Locate every blood parasite and identify its species.
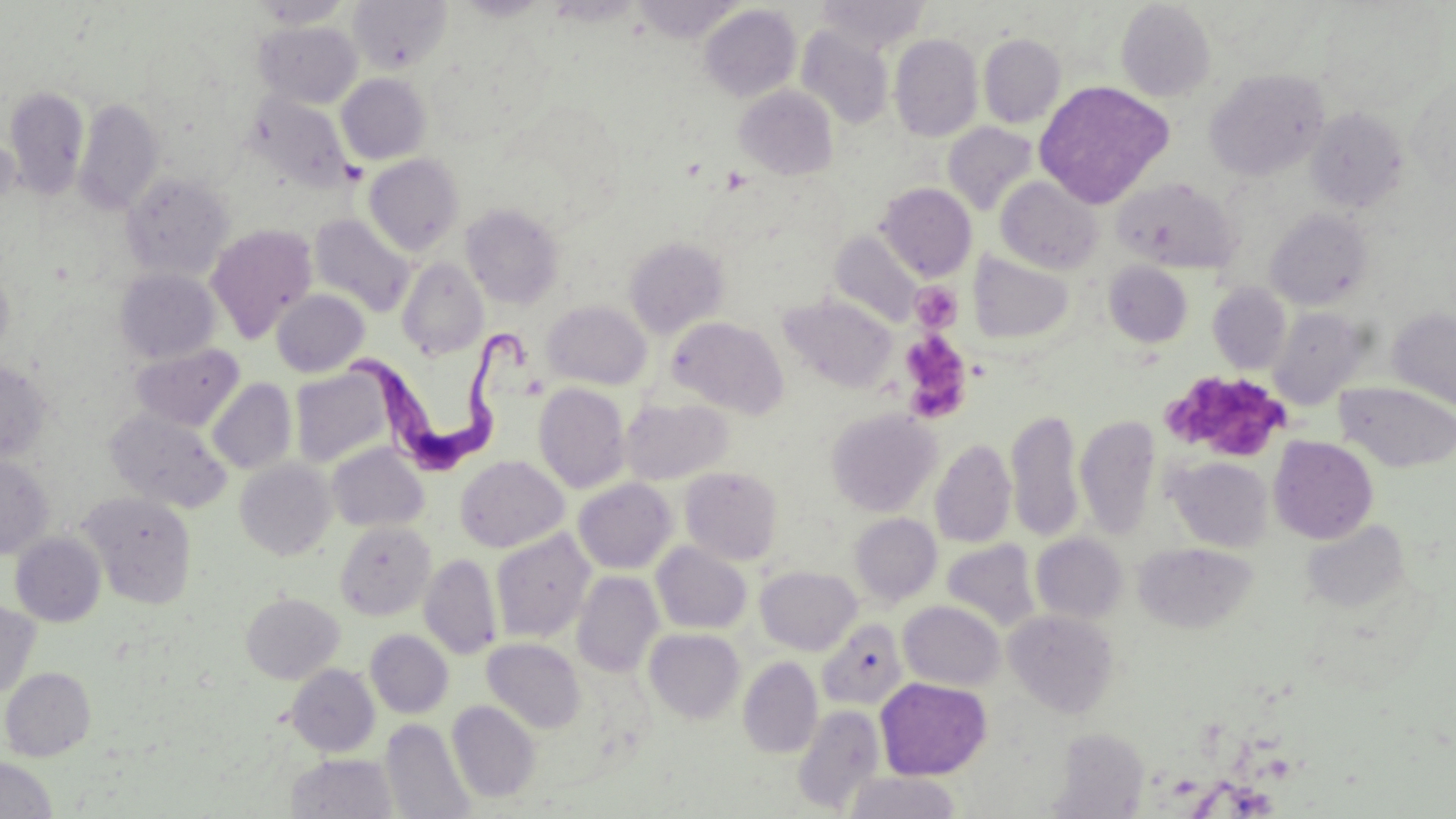

Approximate bounding boxes as (x1, y1, x2, y2) in pixels.
Trypanosoma brucei: (349, 321, 534, 475).
No Plasmodium falciparum, Plasmodium ovale, Plasmodium malariae, Plasmodium vivax, or Babesia divergens observed.

Summary:
  - Platelet locations: (909, 281, 962, 333), (898, 333, 972, 422), (1161, 373, 1294, 455)
  - Uninfected red blood cell locations: (348, 0, 452, 74), (633, 0, 746, 42), (818, 1, 931, 53), (1115, 1, 1215, 102), (699, 4, 801, 103), (1316, 4, 1445, 111), (254, 20, 363, 108), (796, 25, 894, 129), (978, 33, 1066, 128), (889, 34, 983, 142), (1204, 69, 1329, 181), (336, 73, 431, 165), (1406, 76, 1455, 190), (1033, 80, 1174, 208), (734, 85, 838, 180), (4, 86, 89, 199), (246, 93, 355, 193), (73, 97, 164, 215), (1306, 107, 1408, 213), (943, 122, 1038, 215), (364, 154, 464, 255), (121, 170, 234, 280), (995, 176, 1103, 274), (1113, 178, 1239, 274), (877, 182, 976, 281), (461, 203, 565, 309), (1266, 209, 1373, 309), (309, 213, 416, 317), (205, 224, 318, 341), (829, 231, 924, 328), (624, 236, 729, 338), (968, 251, 1076, 344), (396, 257, 489, 360), (1104, 261, 1193, 347), (0, 267, 13, 361), (115, 268, 220, 364), (1207, 282, 1292, 374), (271, 289, 369, 377), (781, 295, 897, 393), (542, 300, 652, 390), (1267, 306, 1372, 409), (1388, 308, 1456, 411), (666, 316, 788, 418), (131, 342, 244, 431), (0, 361, 53, 464), (290, 368, 393, 468), (207, 378, 297, 475), (1335, 381, 1456, 472), (533, 382, 630, 493), (620, 397, 732, 485), (825, 408, 941, 517), (1007, 408, 1084, 543), (106, 409, 231, 513), (1075, 414, 1160, 539), (1268, 436, 1378, 544), (930, 438, 1017, 548), (326, 443, 429, 532), (0, 455, 54, 559), (455, 455, 569, 553), (1166, 456, 1273, 552), (235, 458, 336, 560), (680, 467, 784, 564), (573, 478, 677, 574), (79, 491, 198, 608), (849, 513, 942, 607), (1300, 519, 1411, 613), (335, 521, 435, 620), (490, 529, 595, 643), (10, 532, 106, 627), (1031, 533, 1127, 624), (941, 538, 1041, 633), (651, 541, 752, 634), (1134, 542, 1258, 634), (419, 553, 502, 659), (756, 566, 862, 655), (572, 571, 663, 678), (241, 592, 344, 684), (0, 600, 40, 700), (898, 601, 1005, 690), (1005, 609, 1120, 718), (816, 619, 908, 710), (644, 628, 746, 723), (365, 629, 453, 718), (482, 638, 586, 733), (738, 656, 823, 758), (286, 664, 380, 757), (1, 667, 96, 761), (875, 677, 991, 780), (448, 700, 541, 802), (792, 705, 885, 814), (381, 718, 475, 819), (1049, 728, 1149, 816), (287, 752, 397, 818), (0, 756, 58, 819), (844, 771, 963, 819)
  - Slide-level diagnosis: Trypanosoma brucei
  - Magnification: 1000x
  - Field of view: one of a larger specimen
  - Preparation: thin blood film
  - Modality: optical microscopy
  - Image size: 1456×819 pixels
  - Stain: May-Grünwald-Giemsa